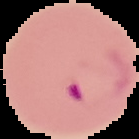

Summary:
  - Preparation: thin blood smear
  - Image size: 139×139 pixels
  - Image type: segmented cell region on a black background
  - Malaria status: parasitized